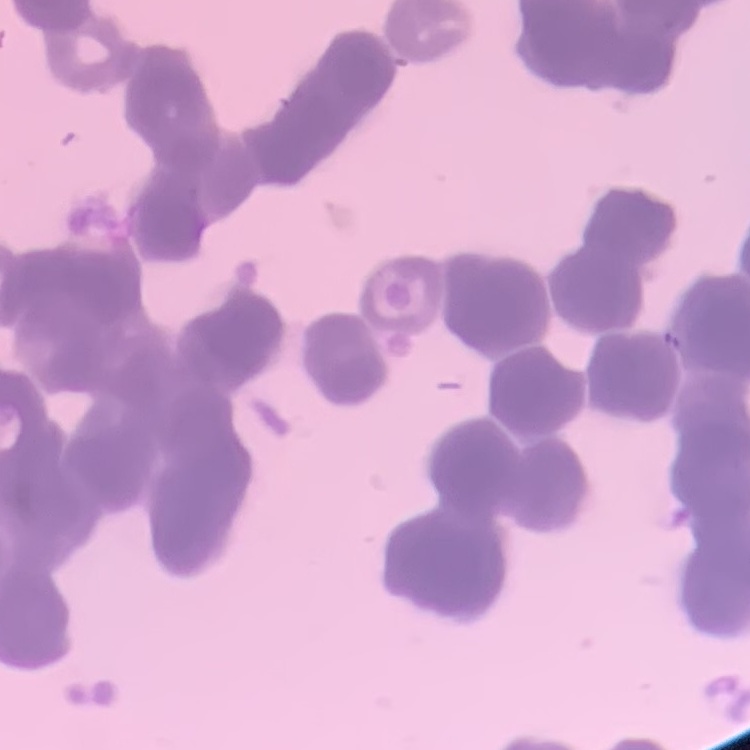
The erythrocytes exhibit rouleaux formation. Square crop of a larger photomicrograph. Field's or Giemsa stain. Thin blood smear.